Report the malaria status of this cell.
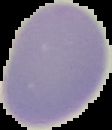

It is uninfected.

Cell region segmented out of the field of view; the surrounding area is masked to black. Image is 112×130 pixels. From a thin blood smear.